Assess this cell for malaria.
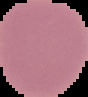
It is uninfected.

Summary:
  - Image type: cell region segmented out of the field of view; surrounding area masked to black
  - Preparation: thin blood film
  - Image size: 88×97 pixels